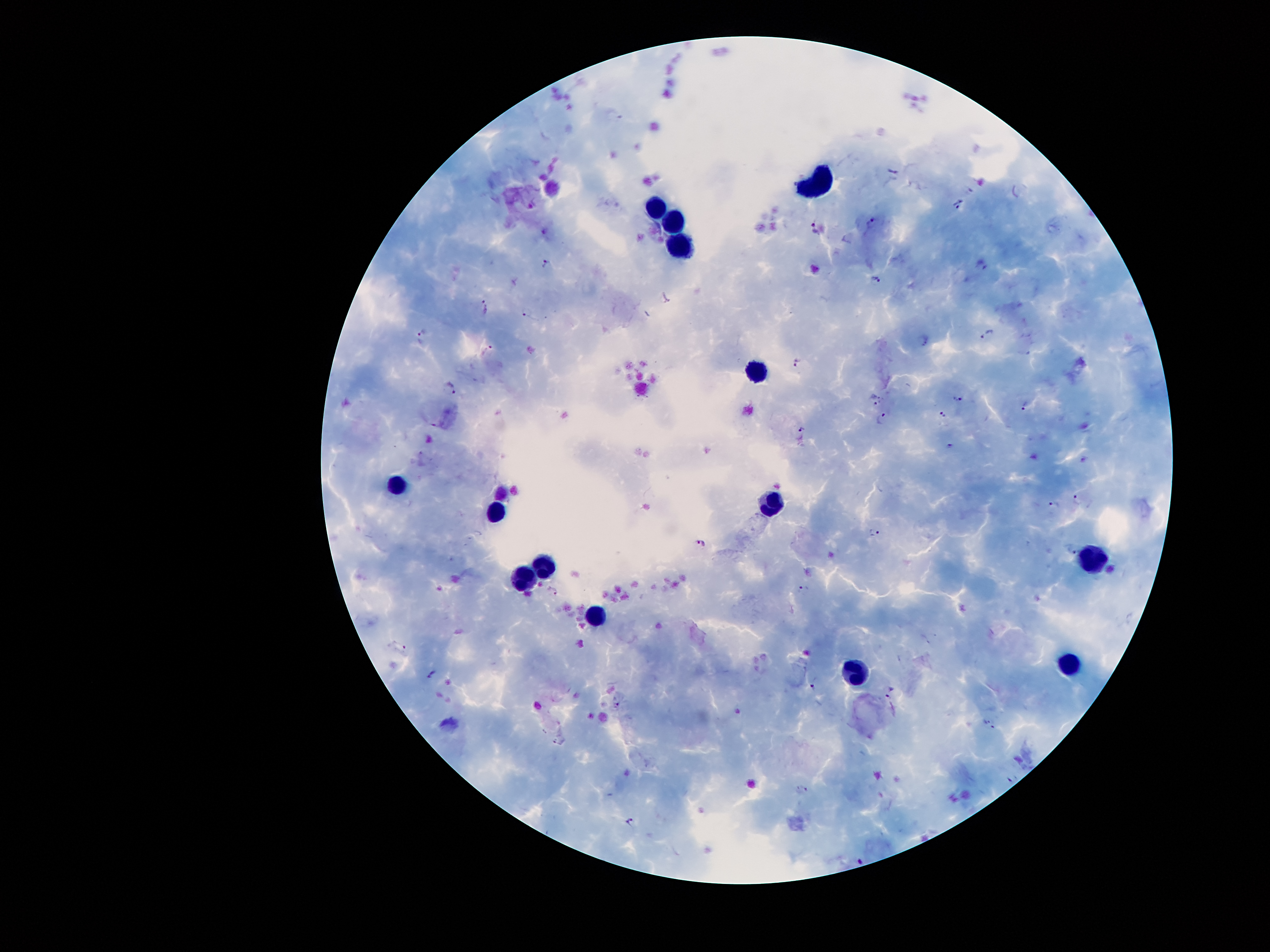
Approximate centers as [x, y] in pixels. Leukocyte locations: [821, 178], [657, 200], [674, 225], [680, 241], [759, 367], [394, 483], [774, 503], [497, 511], [1090, 562], [541, 567], [520, 579], [593, 618], [1073, 662], [855, 669]. Plasmodium parasite locations: [895, 172], [960, 206], [871, 222], [816, 225], [548, 264], [982, 264], [876, 279], [666, 299], [487, 307], [526, 312], [423, 332], [988, 333], [487, 350], [1025, 352], [796, 362], [450, 387], [958, 397], [874, 399], [1025, 405], [945, 413], [881, 417], [802, 429], [951, 444], [1077, 499], [1053, 505], [874, 531], [699, 542], [1073, 551], [801, 588], [553, 591], [402, 647], [431, 673], [813, 688], [892, 693], [618, 705], [987, 721], [994, 726], [1013, 778], [802, 789], [630, 818]. Giemsa-stained preparation. Thick blood film. Image is 1270×952 pixels. One field from this slide. Smartphone photograph taken through the microscope eyepiece. 100x magnification. Patient malaria status: infected with Plasmodium falciparum.